Locate and identify every blood parasite.
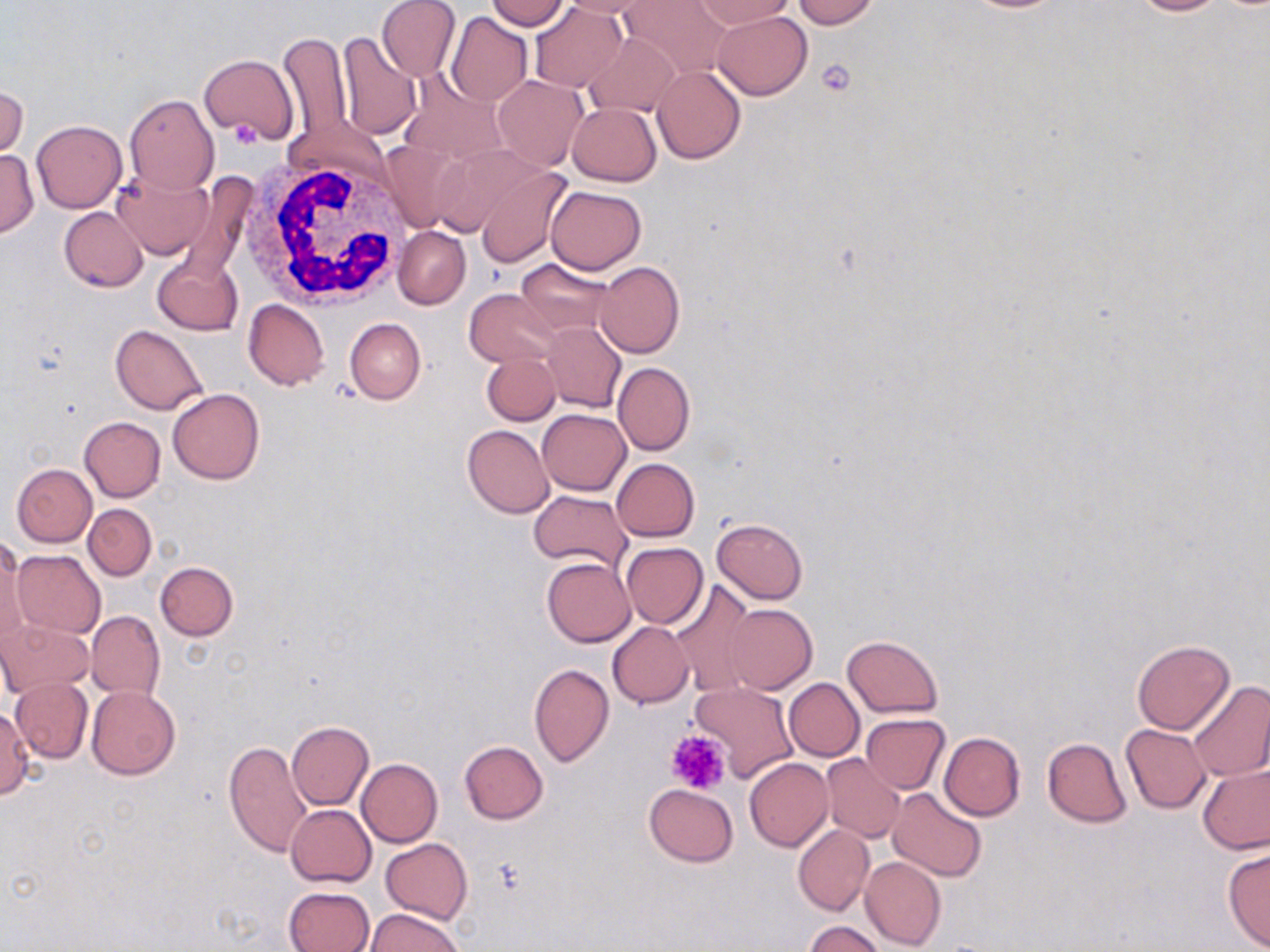
No blood parasites observed.

Summary:
  - Coordinate format: approximate bounding boxes as [x1, y1, x2, y2] in pixels
  - Platelet locations: [816, 60, 856, 97], [666, 730, 730, 795]
  - White blood cell locations: [244, 152, 410, 309]
  - Uninfected red blood cell locations: [376, 0, 459, 82], [483, 0, 570, 31], [560, 0, 659, 17], [624, 0, 732, 79], [690, 0, 796, 30], [791, 0, 879, 28], [1122, 0, 1228, 17], [530, 2, 626, 93], [446, 12, 532, 106], [712, 12, 811, 100], [278, 32, 353, 143], [334, 32, 422, 141], [583, 32, 679, 116], [199, 54, 298, 143], [653, 65, 745, 164], [399, 72, 508, 164], [493, 75, 588, 171], [1, 83, 28, 160], [124, 94, 218, 194], [567, 103, 661, 186], [31, 120, 128, 213], [377, 140, 464, 231], [0, 150, 38, 237], [475, 164, 572, 268], [113, 168, 214, 258], [546, 185, 646, 274], [59, 207, 148, 292], [394, 226, 471, 310], [153, 253, 243, 336], [516, 258, 614, 337], [595, 262, 685, 358], [465, 289, 563, 368], [243, 299, 329, 390], [345, 318, 425, 404], [541, 322, 626, 413], [110, 326, 208, 414], [481, 353, 561, 426], [613, 362, 695, 455], [168, 388, 264, 484], [536, 408, 631, 495], [79, 416, 166, 501], [462, 425, 554, 518], [612, 458, 699, 541], [11, 463, 97, 546], [529, 491, 632, 571], [84, 504, 156, 581], [711, 517, 808, 604], [0, 539, 27, 643], [620, 542, 708, 628], [12, 548, 106, 638], [543, 557, 635, 646], [155, 561, 238, 640], [668, 581, 758, 695], [723, 603, 817, 693], [85, 609, 165, 700], [0, 620, 95, 697], [608, 621, 693, 707], [841, 635, 944, 718], [1132, 640, 1234, 734], [528, 664, 614, 766], [784, 678, 864, 761], [12, 679, 92, 761], [690, 679, 797, 781], [1187, 682, 1270, 782], [87, 686, 180, 780], [0, 705, 34, 800], [860, 714, 951, 793], [286, 721, 373, 810], [1121, 724, 1212, 813], [939, 732, 1025, 820], [1043, 737, 1132, 827], [222, 738, 311, 858], [459, 741, 548, 824], [822, 754, 905, 843], [744, 758, 833, 851], [357, 759, 443, 847], [1198, 763, 1270, 854], [644, 784, 739, 865], [887, 787, 988, 882], [286, 804, 375, 887], [793, 824, 874, 916], [381, 838, 472, 926], [1222, 847, 1270, 950], [859, 857, 946, 951], [283, 886, 375, 952], [366, 909, 464, 952], [804, 921, 886, 952]
  - Slide-level diagnosis: negative for blood parasites
  - Stain: May-Grünwald-Giemsa
  - Magnification: 1000x
  - Modality: light microscopy
  - Image size: 1270×952 pixels
  - Preparation: thin blood film
  - Field of view: single